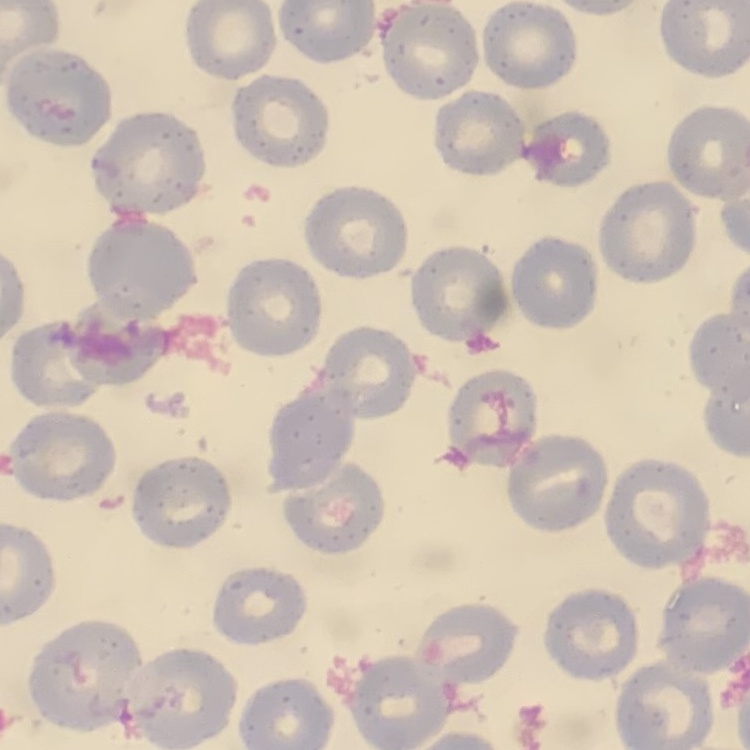

erythrocyte morphology = no rouleaux formation
stain = Field's or Giemsa
image type = one tile cut from a larger photomicrograph
preparation = thin blood film